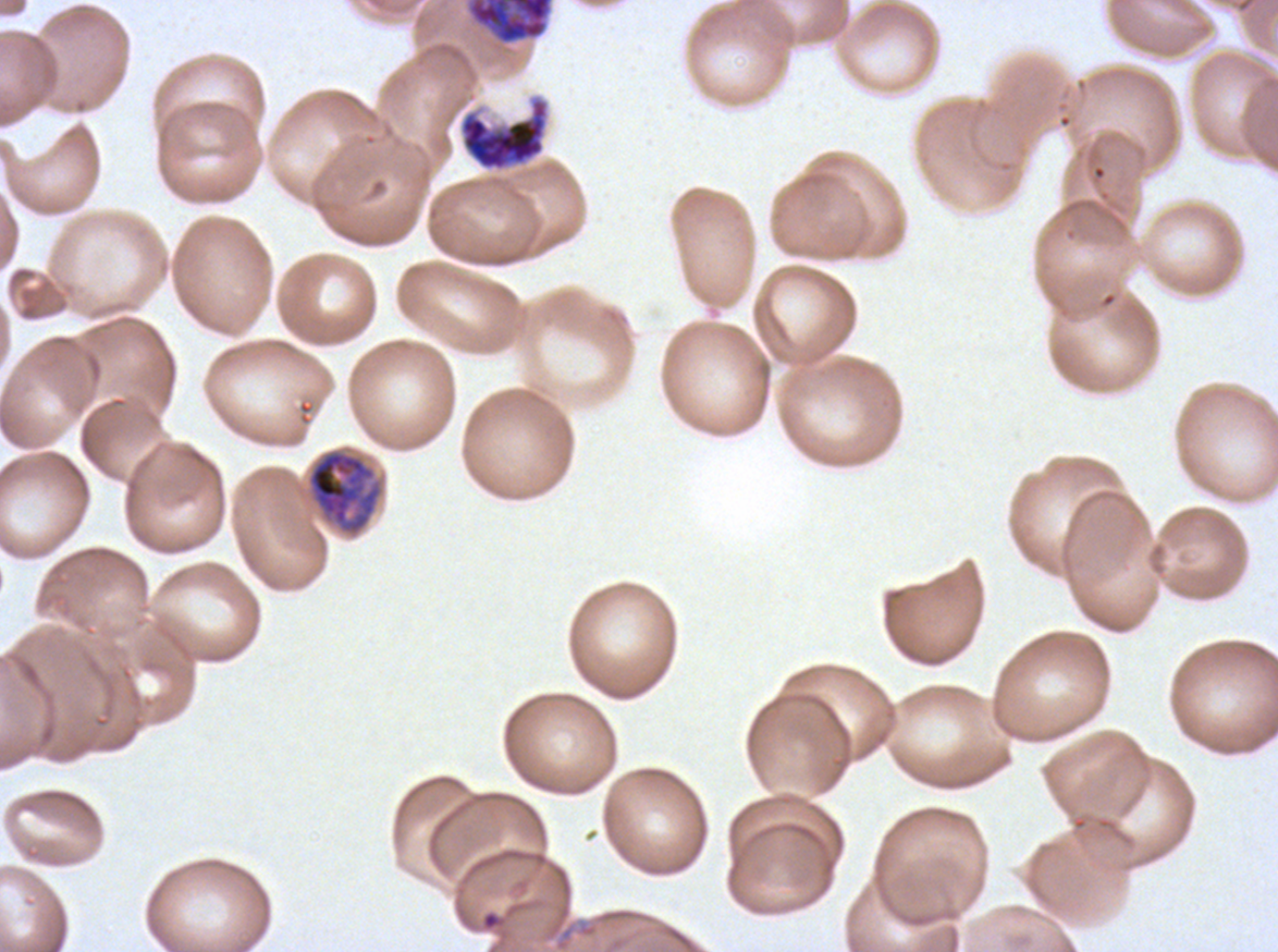
Approximate bounding rectangles given as corner coordinates in pixels from the top-left.
Summary:
  - Late schizont locations: (x1=468, y1=0, x2=552, y2=44), (x1=458, y1=95, x2=550, y2=172)
  - Early schizont locations: (x1=306, y1=449, x2=383, y2=535)
  - Specimen: ex-vivo P. falciparum culture from a patient in The Gambia, grown for 24 to 48 hours
  - Preparation: thin blood film
  - Stain: Giemsa
  - Field of view: sub-image separated from a larger composite
  - Life-cycle stages observed: early schizont, late schizont
  - Image size: 1278×952 pixels